Assess this cell for malaria.
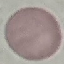
It is uninfected.

Summary:
  - Capture: smartphone through the microscope eyepiece
  - Image type: cell patch, automatically extracted from a larger field of view and resized to 64 × 64 pixels
  - Preparation: thin smear
  - Stain: Giemsa